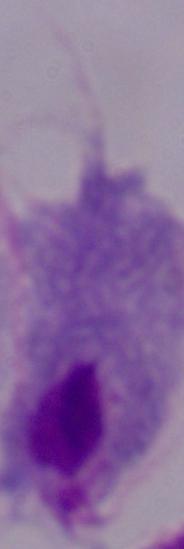 Captured at 1000x magnification. Micrograph. A trichomonad is seen.